Mark where platelets are.
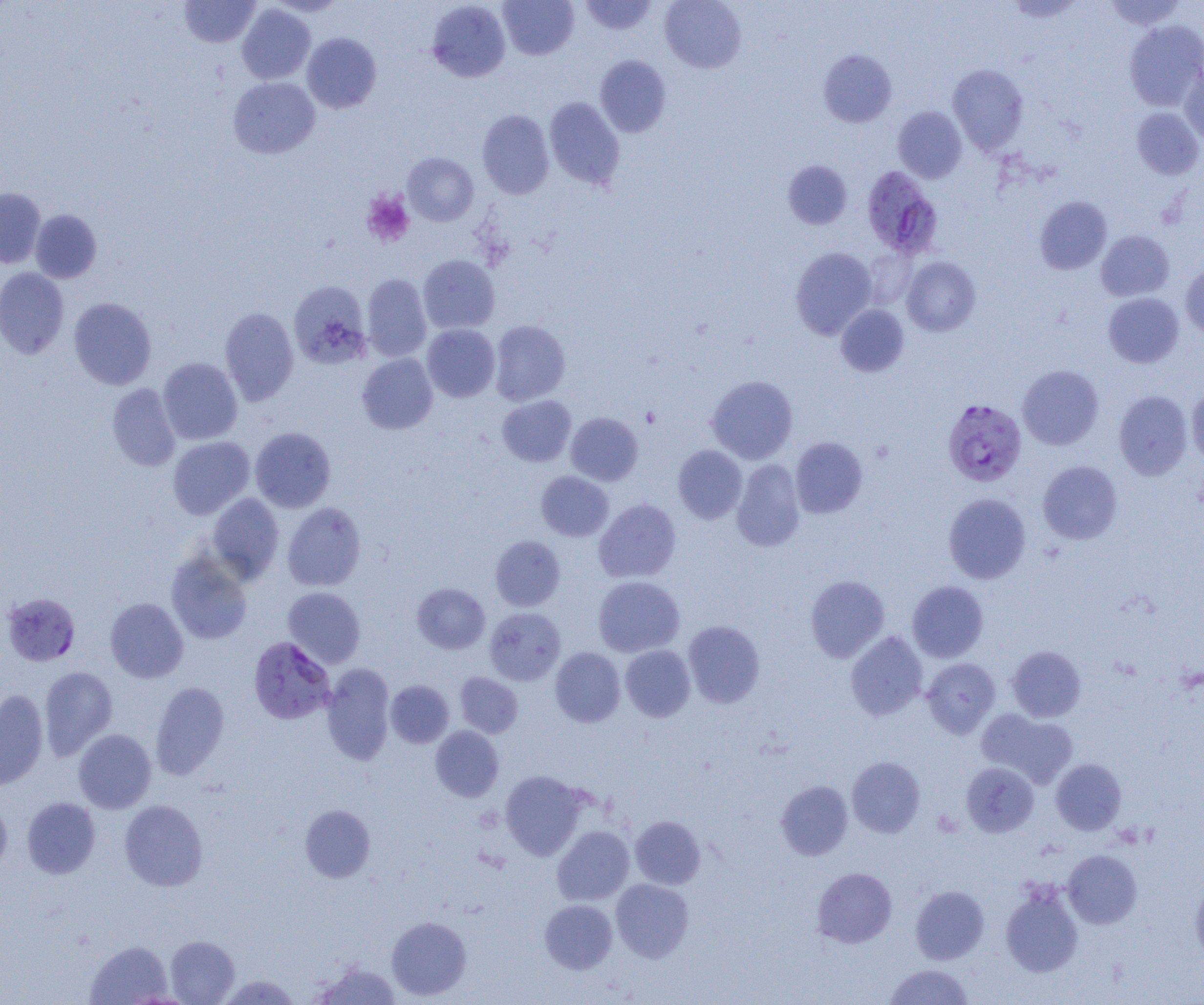
Approximate bounding boxes as named x1/y1/x2/y2 corners in pixels.
Platelets: (x1=362, y1=190, x2=415, y2=247).

Plasmodium falciparum-infected red blood cell locations = approximate bounding boxes as named x1/y1/x2/y2 corners in pixels: (x1=861, y1=166, x2=941, y2=258), (x1=942, y1=398, x2=1027, y2=487), (x1=2, y1=592, x2=80, y2=666), (x1=248, y1=636, x2=336, y2=724)
slide-level diagnosis = Plasmodium falciparum
uninfected red blood cell locations = approximate bounding boxes as named x1/y1/x2/y2 corners in pixels: (x1=179, y1=0, x2=260, y2=47), (x1=264, y1=0, x2=348, y2=17), (x1=498, y1=0, x2=578, y2=60), (x1=579, y1=0, x2=657, y2=35), (x1=660, y1=0, x2=746, y2=73), (x1=1005, y1=0, x2=1084, y2=23), (x1=1105, y1=0, x2=1185, y2=30), (x1=426, y1=1, x2=511, y2=82), (x1=237, y1=4, x2=316, y2=84), (x1=1124, y1=20, x2=1204, y2=111), (x1=302, y1=33, x2=381, y2=113), (x1=818, y1=49, x2=896, y2=127), (x1=595, y1=55, x2=671, y2=137), (x1=947, y1=64, x2=1029, y2=154), (x1=1179, y1=64, x2=1204, y2=143), (x1=228, y1=77, x2=320, y2=159), (x1=544, y1=97, x2=625, y2=190), (x1=893, y1=106, x2=967, y2=183), (x1=1132, y1=107, x2=1203, y2=179), (x1=477, y1=110, x2=554, y2=199), (x1=403, y1=153, x2=479, y2=226), (x1=783, y1=160, x2=852, y2=229), (x1=0, y1=187, x2=45, y2=268), (x1=1034, y1=196, x2=1112, y2=274), (x1=30, y1=209, x2=102, y2=283), (x1=1096, y1=230, x2=1174, y2=301), (x1=791, y1=247, x2=877, y2=339), (x1=861, y1=248, x2=918, y2=308), (x1=418, y1=254, x2=500, y2=334), (x1=902, y1=256, x2=980, y2=336), (x1=1180, y1=263, x2=1204, y2=339), (x1=0, y1=267, x2=69, y2=358), (x1=361, y1=274, x2=431, y2=361), (x1=288, y1=281, x2=371, y2=369), (x1=1103, y1=293, x2=1184, y2=367), (x1=68, y1=297, x2=157, y2=390), (x1=836, y1=304, x2=909, y2=377), (x1=219, y1=306, x2=299, y2=406), (x1=489, y1=320, x2=570, y2=406), (x1=422, y1=324, x2=500, y2=402), (x1=357, y1=353, x2=438, y2=434), (x1=158, y1=357, x2=243, y2=444), (x1=1017, y1=364, x2=1104, y2=450), (x1=706, y1=375, x2=798, y2=463), (x1=107, y1=383, x2=181, y2=472), (x1=1187, y1=386, x2=1204, y2=465), (x1=1113, y1=390, x2=1193, y2=480), (x1=497, y1=395, x2=576, y2=467), (x1=566, y1=412, x2=643, y2=486), (x1=250, y1=427, x2=336, y2=512), (x1=168, y1=436, x2=255, y2=519), (x1=790, y1=437, x2=868, y2=518), (x1=673, y1=445, x2=747, y2=523), (x1=731, y1=459, x2=805, y2=551), (x1=1038, y1=460, x2=1122, y2=544), (x1=536, y1=471, x2=613, y2=541), (x1=207, y1=493, x2=284, y2=584), (x1=943, y1=493, x2=1031, y2=584), (x1=594, y1=498, x2=681, y2=583), (x1=282, y1=502, x2=366, y2=591), (x1=490, y1=536, x2=565, y2=611), (x1=166, y1=551, x2=252, y2=644), (x1=805, y1=575, x2=889, y2=662), (x1=593, y1=576, x2=685, y2=657), (x1=907, y1=581, x2=988, y2=662), (x1=412, y1=583, x2=490, y2=654), (x1=283, y1=587, x2=365, y2=668), (x1=105, y1=597, x2=189, y2=683), (x1=484, y1=607, x2=565, y2=685), (x1=683, y1=620, x2=765, y2=708), (x1=845, y1=631, x2=928, y2=720), (x1=620, y1=645, x2=695, y2=722), (x1=1007, y1=646, x2=1086, y2=722), (x1=550, y1=647, x2=625, y2=727), (x1=922, y1=658, x2=1000, y2=738), (x1=321, y1=664, x2=395, y2=766), (x1=39, y1=666, x2=118, y2=760), (x1=455, y1=673, x2=522, y2=738), (x1=386, y1=680, x2=454, y2=748), (x1=150, y1=681, x2=230, y2=780), (x1=0, y1=689, x2=49, y2=790), (x1=978, y1=709, x2=1078, y2=789), (x1=431, y1=726, x2=504, y2=802), (x1=73, y1=729, x2=156, y2=813), (x1=847, y1=757, x2=925, y2=837), (x1=1051, y1=759, x2=1126, y2=835), (x1=961, y1=762, x2=1039, y2=836), (x1=500, y1=770, x2=588, y2=860), (x1=776, y1=781, x2=853, y2=860), (x1=0, y1=797, x2=12, y2=878), (x1=22, y1=797, x2=100, y2=879), (x1=119, y1=799, x2=208, y2=891), (x1=300, y1=804, x2=376, y2=883), (x1=631, y1=816, x2=705, y2=889), (x1=552, y1=826, x2=634, y2=905), (x1=1062, y1=850, x2=1142, y2=928), (x1=812, y1=867, x2=897, y2=947), (x1=1190, y1=876, x2=1204, y2=963), (x1=611, y1=878, x2=694, y2=962), (x1=1000, y1=882, x2=1083, y2=977), (x1=910, y1=885, x2=989, y2=964), (x1=540, y1=900, x2=617, y2=973), (x1=387, y1=916, x2=471, y2=1000), (x1=165, y1=935, x2=239, y2=1004), (x1=85, y1=940, x2=173, y2=1004), (x1=313, y1=960, x2=401, y2=1004), (x1=884, y1=964, x2=975, y2=1004), (x1=217, y1=974, x2=302, y2=1004)
preparation = thin blood smear
modality = optical microscopy
magnification = 1000x
image size = 1204×1005 pixels
field of view = single